Outline each P. falciparum parasite and classify it by life-cycle stage.
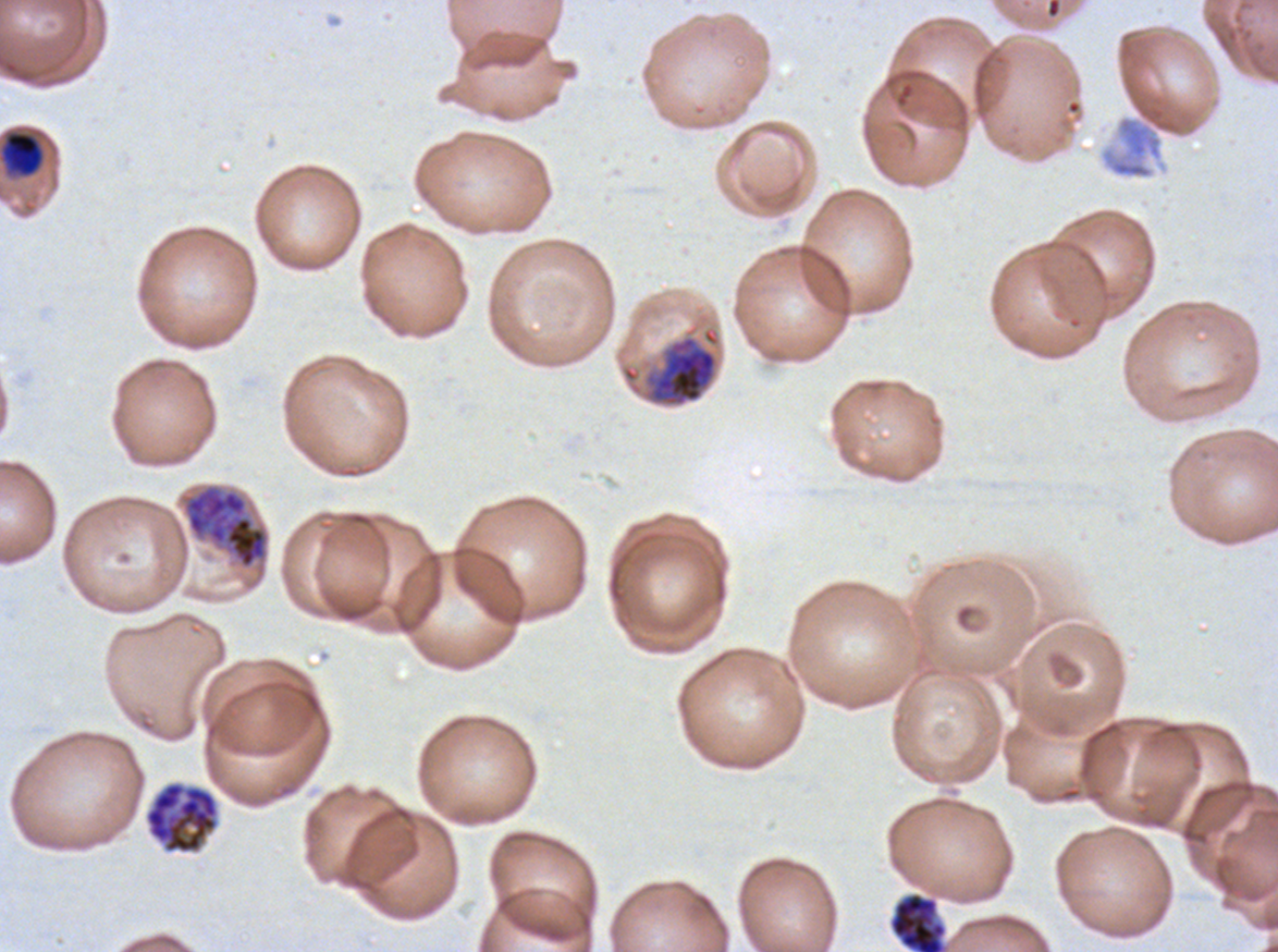

Approximate bounding boxes as [x1, y1, x2, y2] in pixels.
Mid trophozoites: [5, 131, 43, 176].
Early schizonts: [183, 484, 268, 569].
Segmenters: [144, 781, 219, 854], [889, 892, 947, 951].
One object is labeled both early schizont and late schizont by the source: [645, 335, 718, 407].
No rings, late-ring/early-trophozoite forms, late trophozoites, or gametocytes observed.

field of view = one sub-image of a larger composite
specimen = P. falciparum from a patient in The Gambia, cultured ex vivo for 24 to 48 hours
stain = Giemsa
image size = 1278×952 pixels
life-cycle stages observed = mid trophozoite, early schizont, segmenter
preparation = thin blood film